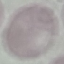
Result: negative for malaria parasites. Automatically extracted cell patch, resized to 64 × 64 pixels. Thin smear of blood. Photographed with a smartphone camera at the microscope eyepiece. Giemsa-stained preparation.